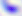
Summary:
  - Modality: micrograph
  - Identification: Toxoplasma gondii
  - Magnification: 400x